Assess this cell for malaria.
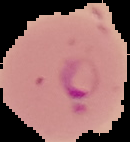

It is parasitized.

Summary:
  - Image type: cell region segmented out of the field of view; surrounding area masked to black
  - Preparation: thin blood film
  - Image size: 130×142 pixels